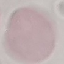

Summary:
  - Malaria status: uninfected
  - Image type: cell patch, automatically extracted from a larger field of view and resized to 64 × 64 pixels
  - Capture: smartphone camera at the microscope eyepiece
  - Stain: Giemsa
  - Preparation: thin smear